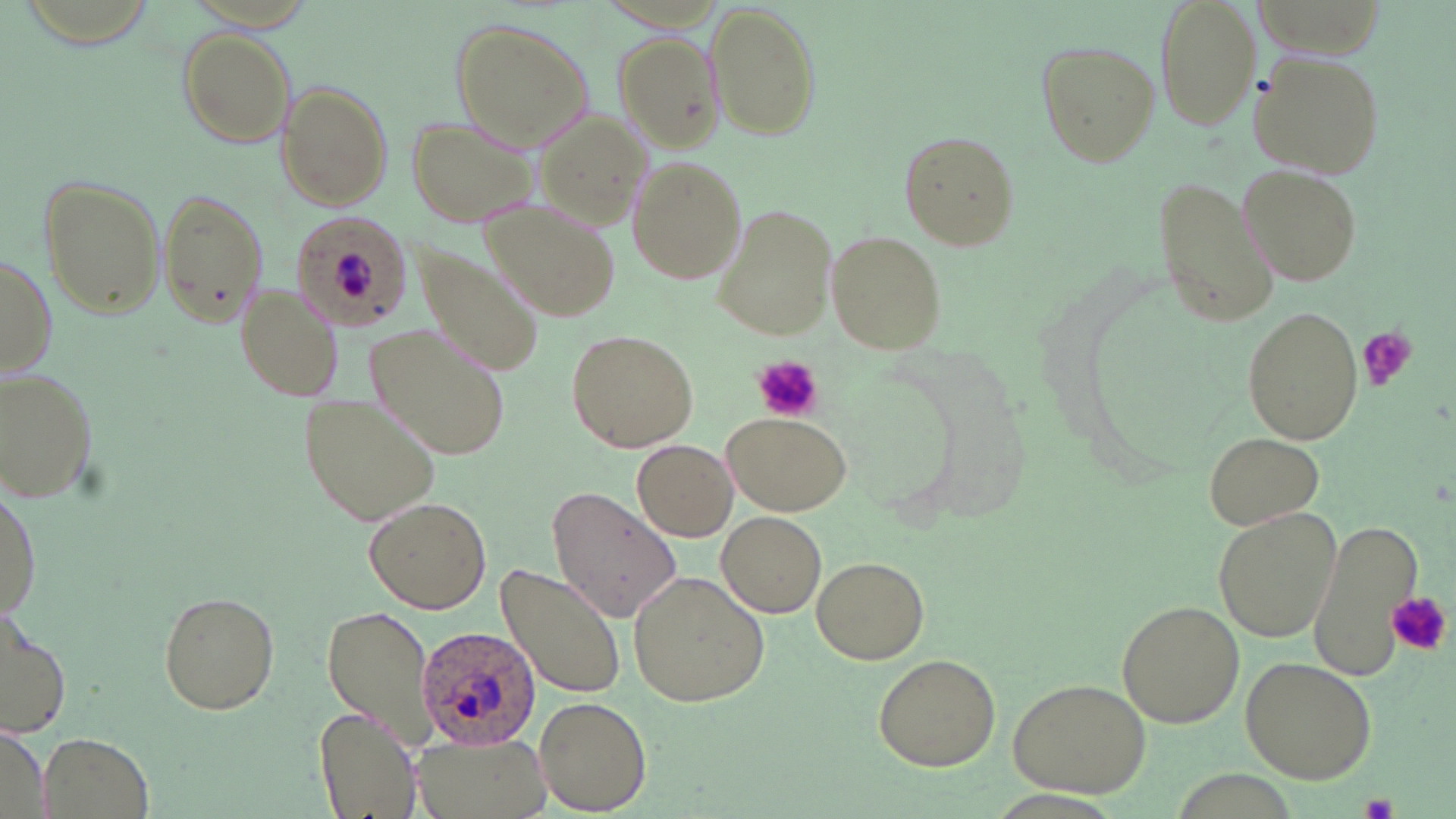
slide-level diagnosis = Plasmodium ovale
uninfected red blood cell locations = approximate bounding boxes as (x1, y1, x2, y2) in pixels: (1153, 0, 1263, 134), (706, 3, 822, 143), (448, 18, 592, 151), (176, 28, 297, 148), (612, 31, 723, 153), (1036, 40, 1160, 168), (1247, 49, 1386, 180), (276, 82, 393, 210), (532, 104, 652, 237), (406, 115, 540, 228), (895, 130, 1022, 250), (627, 157, 745, 284), (1240, 165, 1363, 285), (39, 172, 167, 321), (1153, 172, 1280, 331), (155, 186, 268, 329), (487, 204, 623, 320), (712, 206, 837, 339), (292, 212, 410, 333), (825, 229, 947, 353), (412, 245, 545, 377), (0, 250, 56, 379), (237, 284, 346, 403), (1241, 308, 1365, 442), (365, 319, 513, 464), (565, 328, 698, 453), (1, 366, 102, 505), (302, 392, 443, 526), (724, 414, 851, 514), (1205, 431, 1325, 530), (632, 440, 737, 541), (1, 483, 41, 622), (546, 488, 680, 625), (364, 497, 491, 613), (1212, 506, 1342, 644), (718, 512, 828, 616), (1307, 515, 1422, 683), (811, 556, 929, 664), (493, 562, 626, 701), (630, 568, 774, 706), (157, 590, 280, 716), (1115, 600, 1244, 729), (320, 604, 442, 748), (0, 610, 73, 741), (874, 653, 1000, 771), (1239, 655, 1377, 784), (1008, 677, 1151, 798), (534, 695, 652, 814), (315, 707, 423, 817), (0, 727, 48, 819), (39, 730, 155, 819), (411, 734, 554, 819)
image size = 1456×819 pixels
preparation = thin blood smear
stain = May-Grünwald-Giemsa
Plasmodium ovale-infected red blood cell locations = approximate bounding boxes as (x1, y1, x2, y2) in pixels: (412, 623, 544, 753)
platelet locations = approximate bounding boxes as (x1, y1, x2, y2) in pixels: (330, 251, 375, 299), (1357, 327, 1417, 392), (749, 355, 823, 422), (1388, 592, 1450, 655), (1363, 799, 1397, 819)
magnification = 1000x
field of view = single
modality = optical microscopy